State which parasite is depicted.
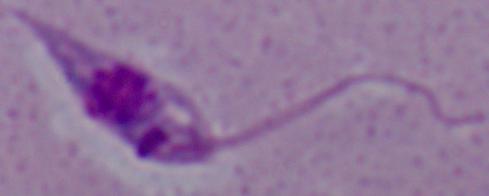

This is Leishmania.

magnification: 1000x
modality: photomicrograph